Classify this cell by malaria status.
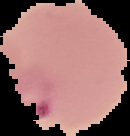

It is parasitized.

Summary:
  - Preparation: thin blood film
  - Image size: 130×136 pixels
  - Image type: segmented cell region with the area outside set to black